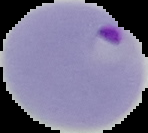
Result: Plasmodium parasites detected. From a thin blood smear. Image is 148×133 pixels. Cell region segmented out of the field of view; the surrounding area is masked to black.